Identify the parasite.
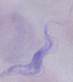
A trypanosome.

Summary:
  - Modality: micrograph
  - Magnification: 1000x